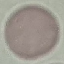
Malaria status: uninfected. Thin blood film. Cell patch, automatically extracted from a larger field of view and resized to 64 × 64 pixels. Giemsa stain. Photographed with a smartphone camera at the microscope eyepiece.